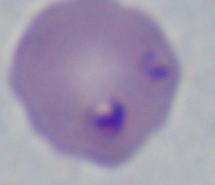
Micrograph. A Babesia parasite is seen. Captured at 1000x magnification.